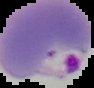 From a thin blood smear. Malaria status: parasitized. Image is 94×88 pixels. Segmented cell region on a black background.